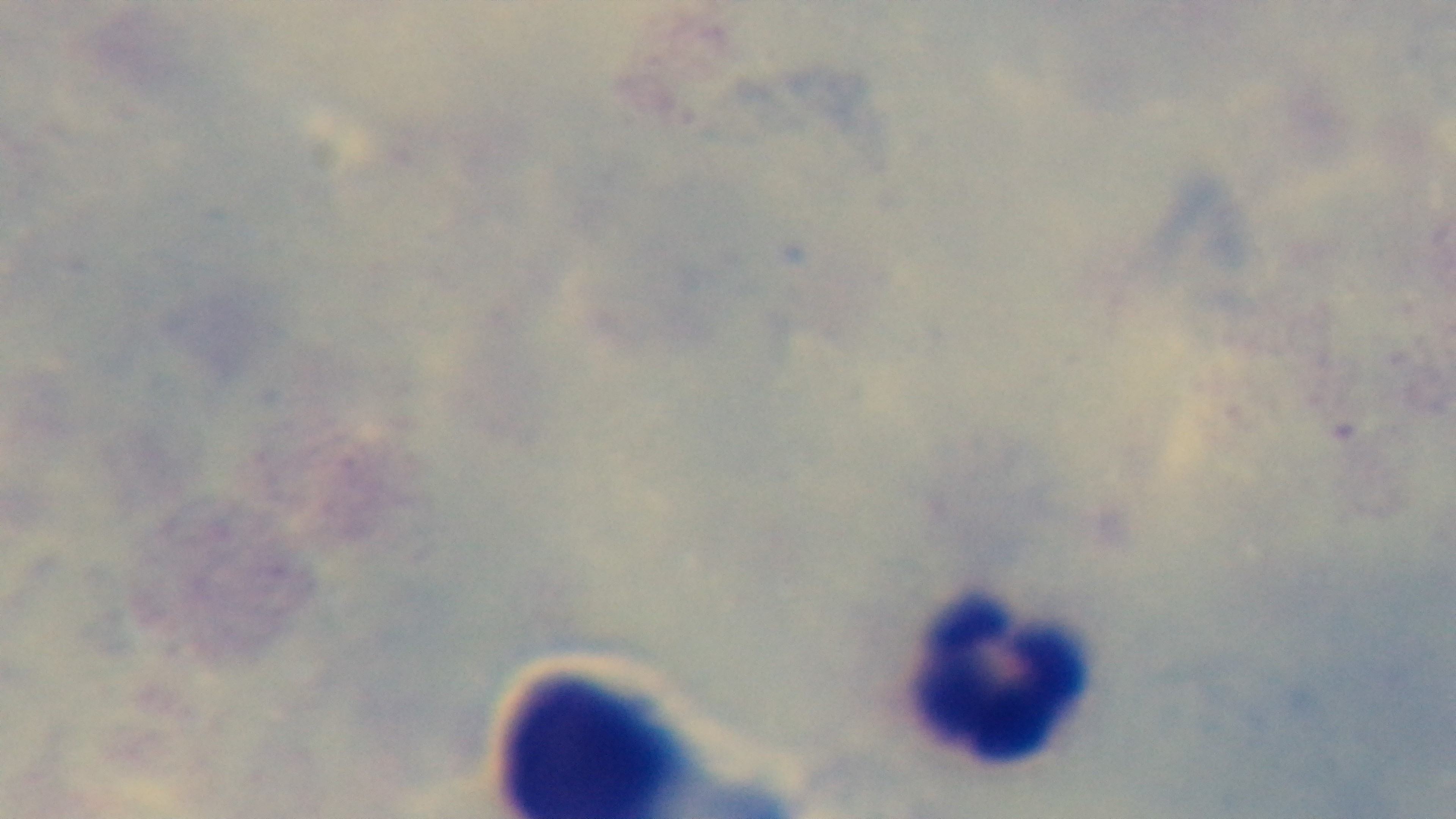
{
  "capture": "mounted 4K digital camera",
  "stain": "Giemsa",
  "preparation": "thick blood film",
  "field_of_view": "one from the slide",
  "modality": "light microscopy",
  "malaria_status": "negative",
  "objective": "100x oil immersion"
}